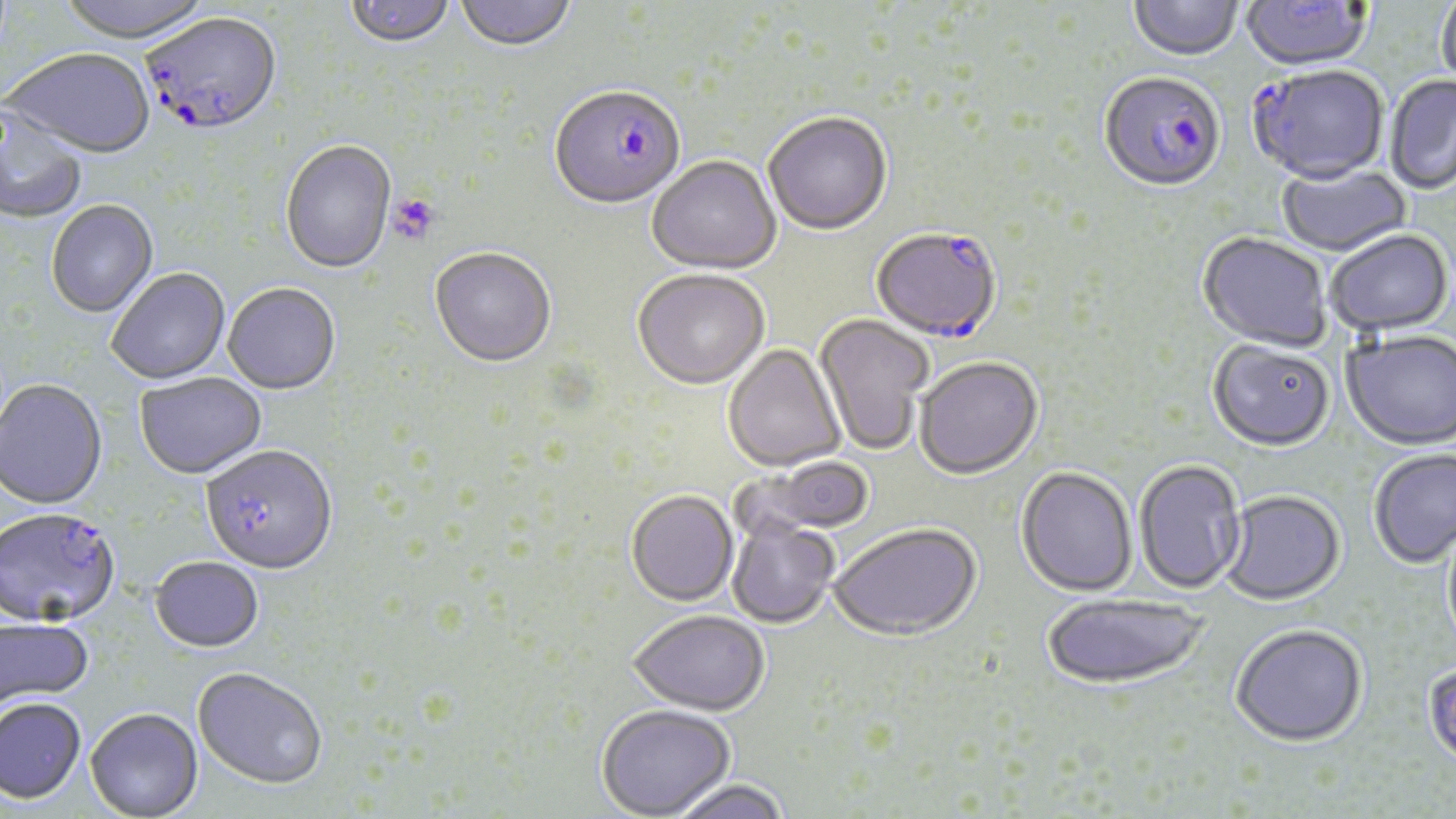
Summary:
  - Coordinate format: approximate bounding boxes as (x1, y1, x2, y2) in pixels
  - Plasmodium falciparum-infected red blood cell locations: (143, 15, 282, 140), (1248, 67, 1389, 188), (1098, 74, 1226, 195), (549, 88, 685, 212), (872, 230, 1002, 345), (201, 448, 337, 577), (0, 510, 120, 630)
  - Uninfected red blood cell locations: (57, 0, 214, 47), (344, 0, 456, 50), (454, 0, 576, 54), (1241, 0, 1372, 74), (1129, 1, 1244, 63), (1435, 1, 1456, 92), (5, 51, 155, 161), (1384, 75, 1456, 195), (0, 105, 88, 225), (764, 114, 892, 237), (280, 142, 397, 275), (647, 157, 782, 277), (1277, 164, 1412, 258), (47, 201, 158, 318), (1326, 231, 1453, 338), (1198, 233, 1331, 354), (429, 250, 556, 370), (107, 270, 230, 385), (633, 271, 770, 392), (222, 285, 341, 397), (813, 314, 933, 456), (1341, 332, 1456, 453), (1207, 342, 1335, 453), (723, 345, 846, 473), (915, 359, 1043, 481), (135, 374, 267, 481), (0, 381, 108, 512), (1368, 451, 1456, 570), (742, 457, 877, 537), (1134, 461, 1246, 596), (1016, 469, 1137, 599), (626, 491, 739, 607), (1219, 492, 1346, 608), (727, 519, 840, 629), (1442, 523, 1456, 661), (829, 524, 982, 643), (150, 558, 264, 655), (1042, 596, 1210, 693), (629, 610, 768, 716), (0, 618, 94, 713), (1230, 627, 1368, 750), (1423, 665, 1456, 774), (192, 669, 327, 792), (0, 700, 86, 807), (595, 705, 736, 818), (85, 710, 203, 819), (666, 780, 793, 819)
  - Platelet locations: (387, 194, 441, 246)
  - Slide-level diagnosis: Plasmodium falciparum
  - Magnification: 1000x
  - Field of view: one of a larger specimen
  - Modality: optical microscopy
  - Stain: May-Grünwald-Giemsa
  - Preparation: thin blood film
  - Image size: 1456×819 pixels